Report the malaria status of this cell.
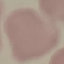
Uninfected.

Summary:
  - Image type: cell patch, automatically extracted from a larger field of view and resized to 64 × 64 pixels
  - Preparation: thin blood film
  - Stain: Giemsa
  - Capture: smartphone through the microscope eyepiece